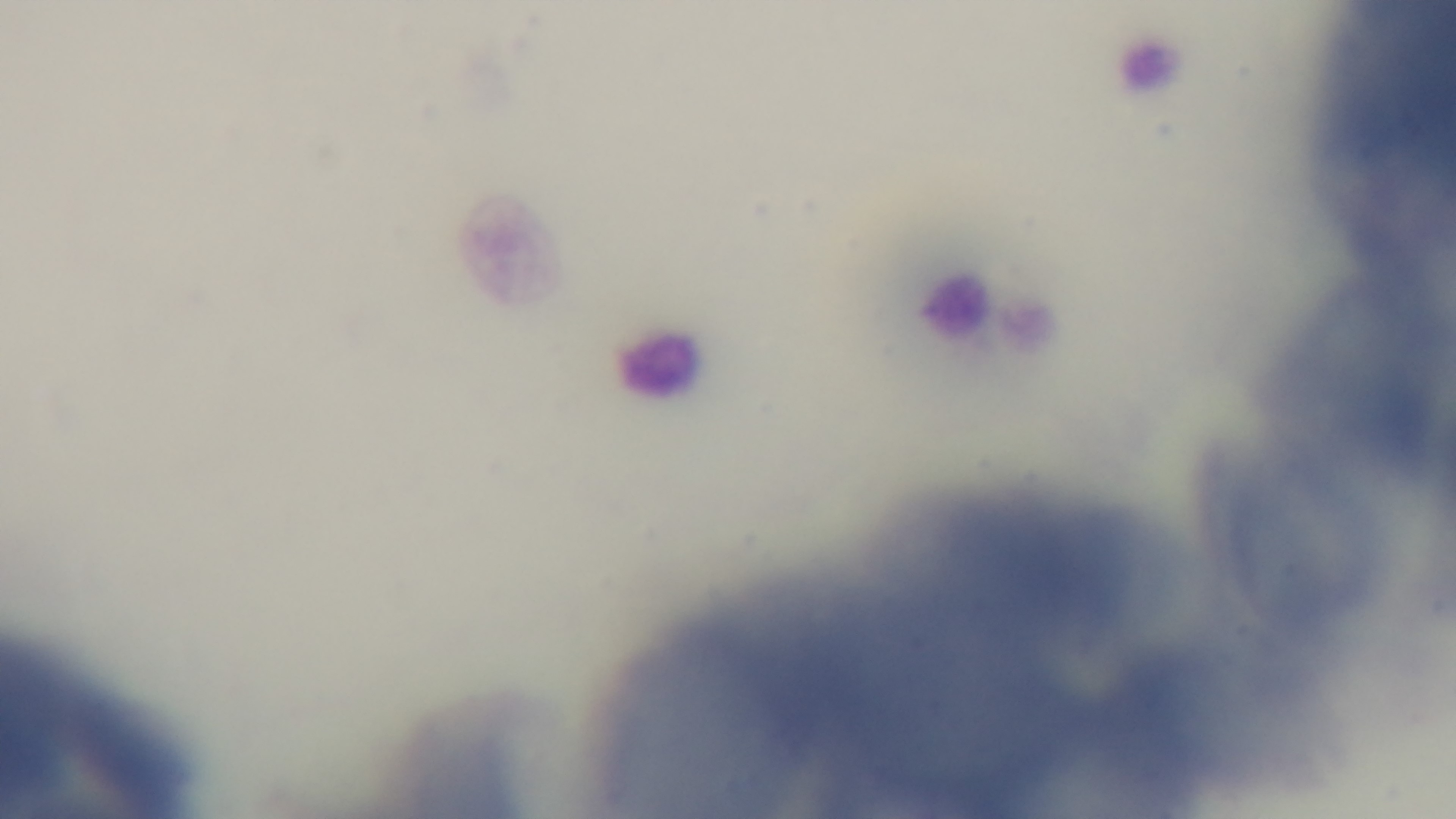

field of view = single
modality = light microscopy
capture = mounted 4K digital camera
stain = Giemsa
objective = 100x oil immersion
preparation = thin blood film
malaria status = uninfected